Identify the parasite.
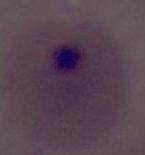
This is Plasmodium.

Photomicrograph. Captured at either 400x or 1000x magnification.